Classify this cell by malaria status.
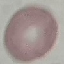

Uninfected.

Acquired by smartphone through the microscope eyepiece. Giemsa stain. Automatically extracted cell patch, resized to 64 × 64 pixels. Thin smear of blood.